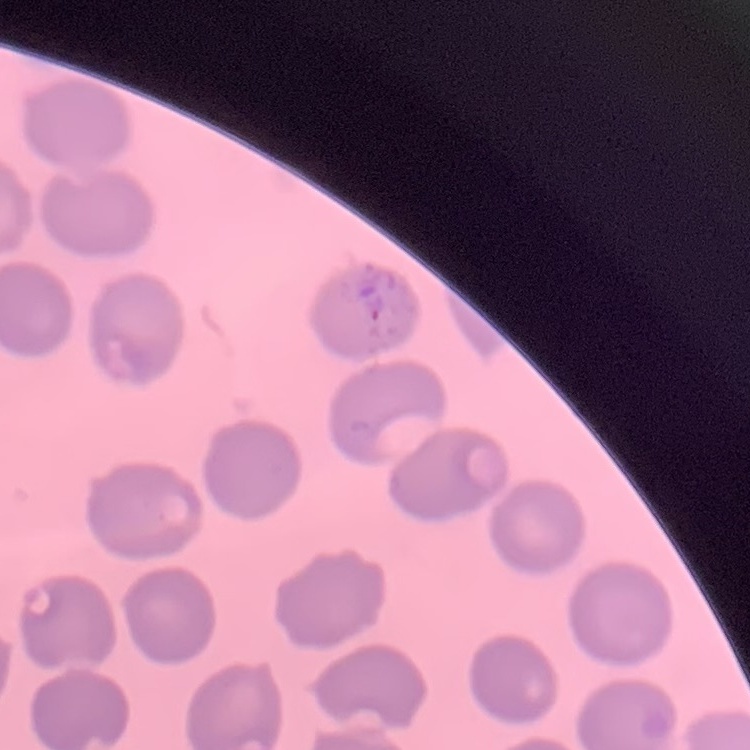 The erythrocytes show no rouleaux formation. Field's or Giemsa stain. One tile cut from a larger photomicrograph. Thin blood smear.